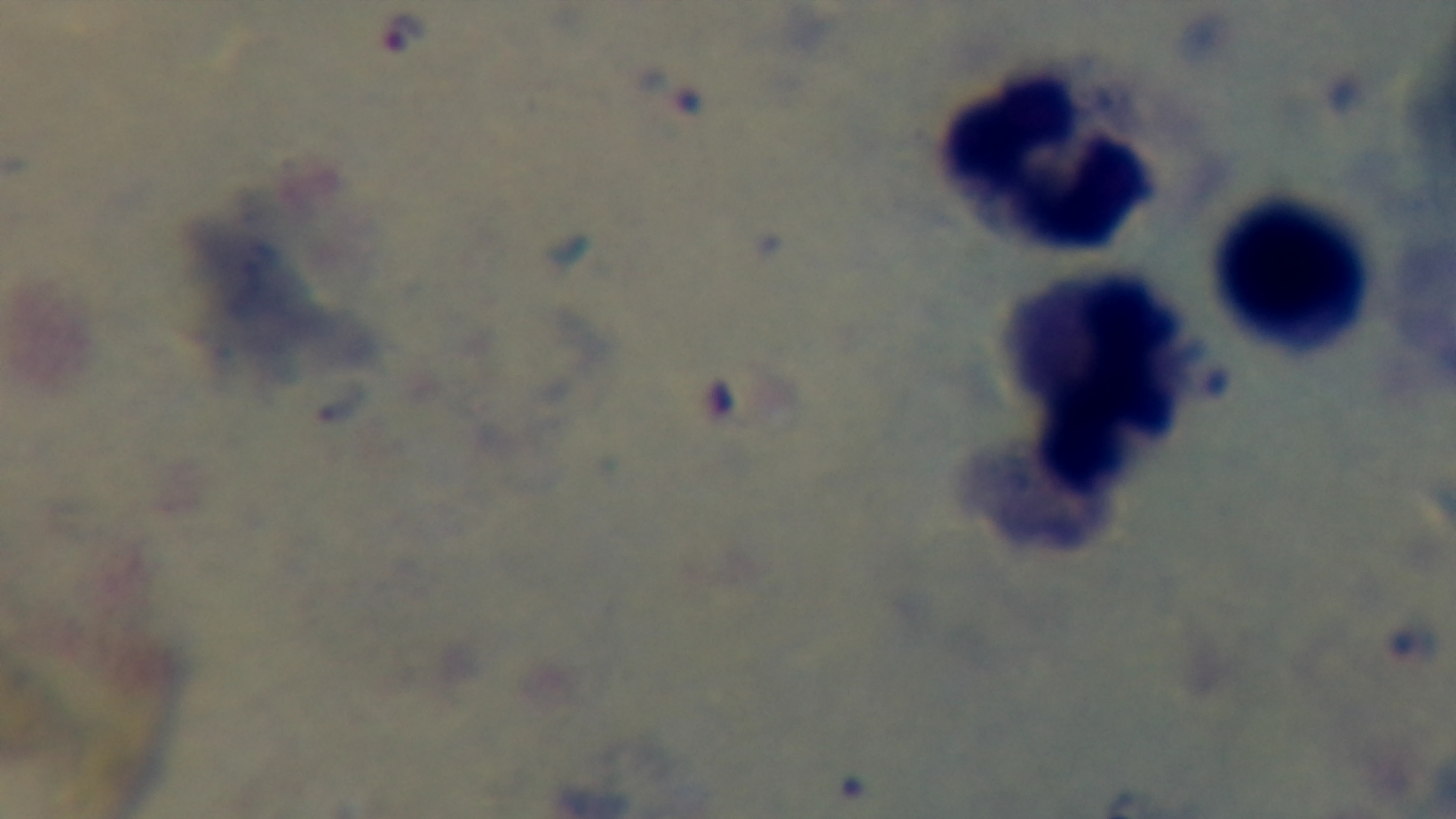 One field from the slide. Light microscopy. Captured with a mounted 4K digital camera. Malaria status: positive. Preparation: thick smear. Giemsa stain. Oil-immersion objective, 100x.